Outline every artifact (platelet-like body, stain precipitate, or debris).
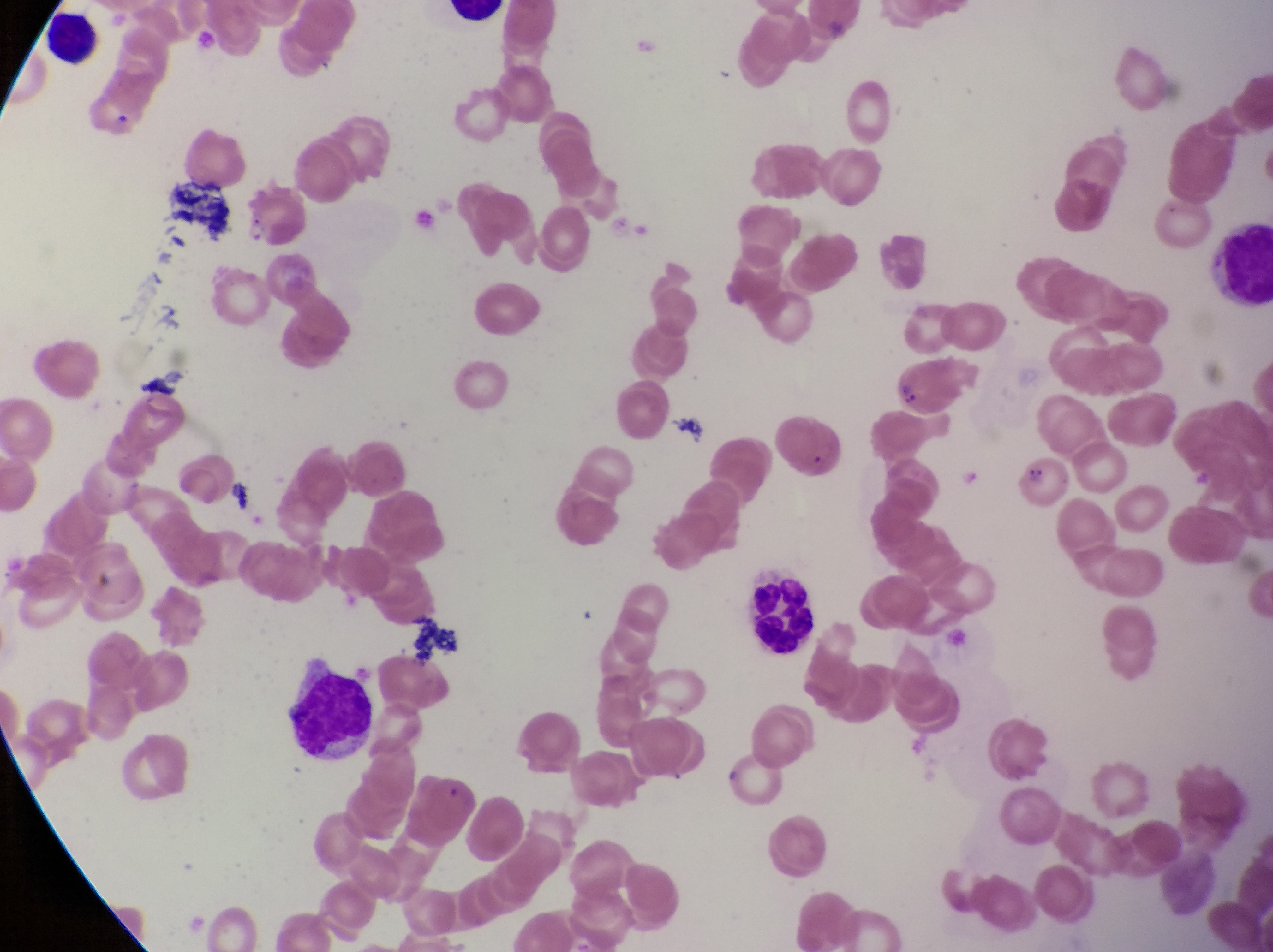
Approximate bounding boxes as left top right bottom in pixels.
Artifacts (platelet-like body, stain precipitate, or debris): 104 102 137 142; 158 177 232 235; 670 412 706 450; 1026 459 1048 491; 409 617 460 667.

image_size: 1273×952 pixels
preparation: thin blood smear
field_of_view: single
leukocyte_locations: 'approximate bounding boxes as left top right bottom in pixels: 34 10 97 68; 1196 223 1270 308; 747 577 824 660; 278 656 377 766'
country: Uganda
magnification: 1000x
capture: smartphone photograph through the eyepiece of an Olympus CX-23 microscope
parasitised_red_blood_cell_locations: 'approximate bounding boxes as left top right bottom in pixels: 888 352 962 415; 776 414 848 484'